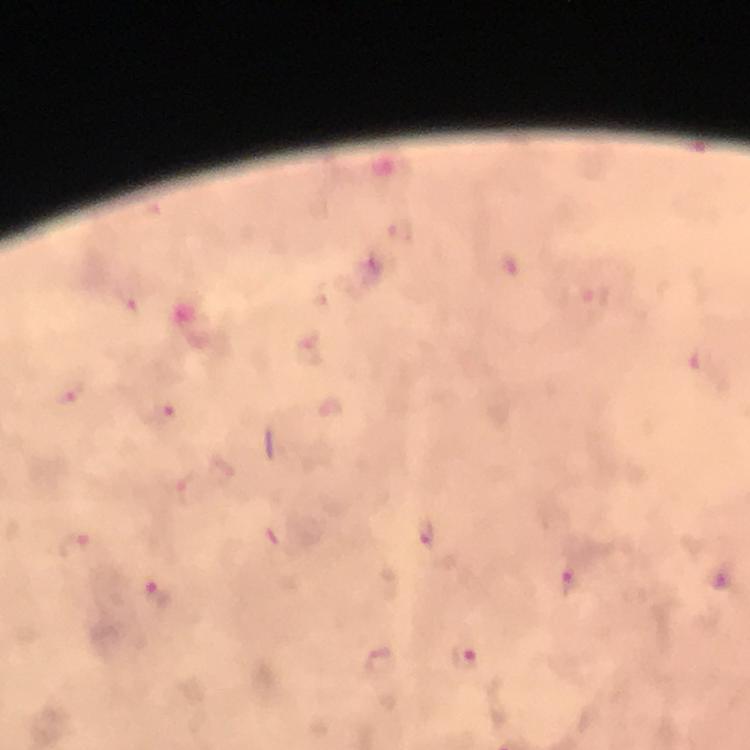

Approximate centers as {x, y} in pixels. Malaria parasite locations: {401, 230}, {511, 263}, {132, 303}, {68, 395}, {158, 415}, {428, 533}, {75, 546}, {720, 576}, {568, 579}, {154, 592}, {466, 653}. Immersion oil was used. Smartphone photograph taken through a microscope. From a diagnostic examination for malaria. Giemsa-stained preparation. Cropped region of a single field of view. Thick blood film. At 100x magnification. Image is 750×750 pixels.